Classify this cell by malaria status.
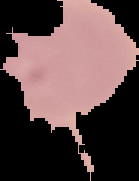
It is uninfected.

Summary:
  - Image type: segmented cell region with the area outside set to black
  - Image size: 139×181 pixels
  - Preparation: thin blood smear